Classify this cell by malaria status.
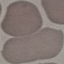
It is uninfected.

Giemsa stain. Thin smear of blood. Automatically extracted cell patch, resized to 64 × 64 pixels. Photographed with a smartphone camera at the microscope eyepiece.